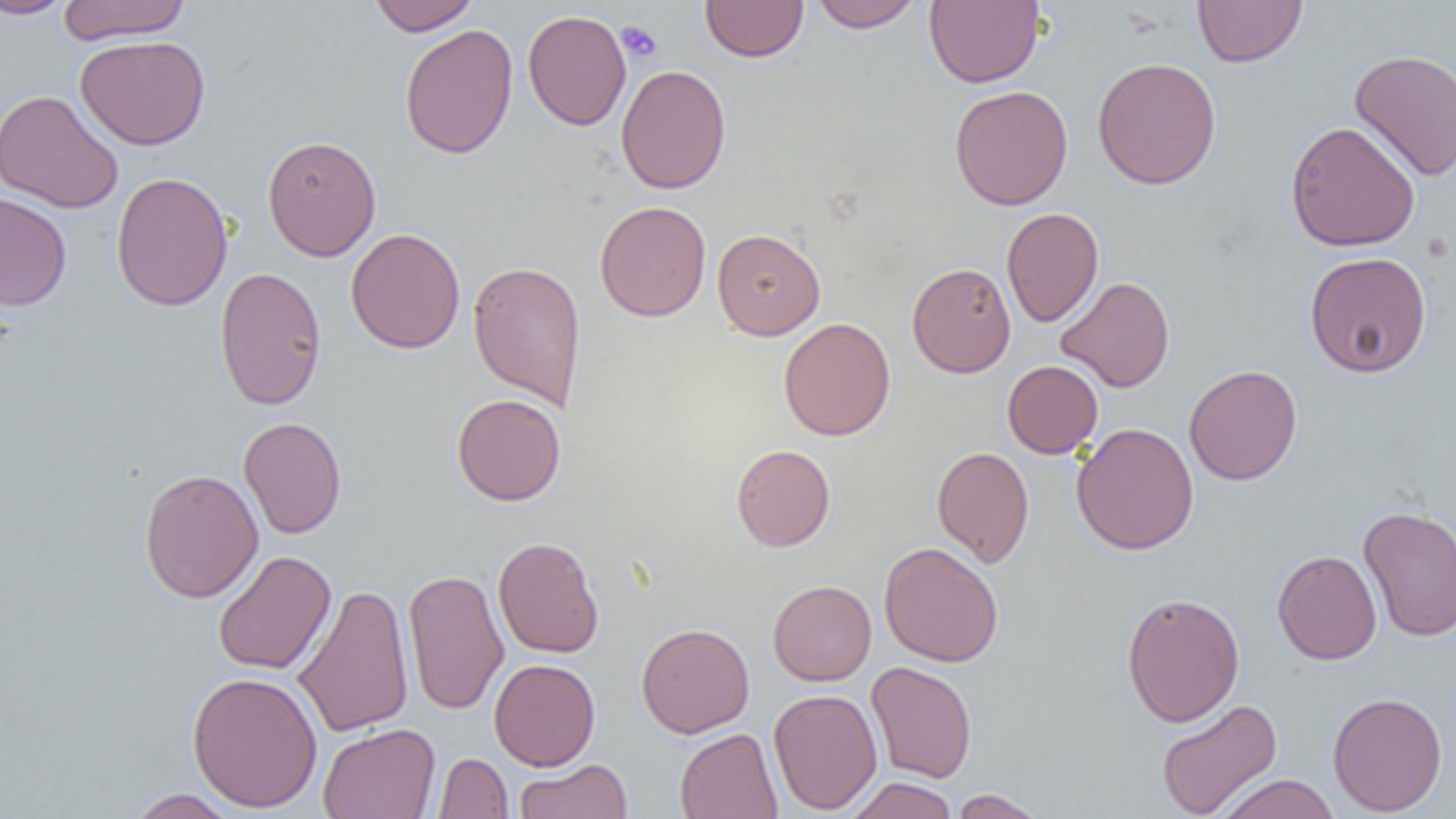

Approximate bounding boxes as [x1, y1, x2, y2] in pixels. Platelet locations: [616, 21, 662, 63]. Uninfected red blood cell locations: [0, 0, 78, 19], [56, 0, 192, 44], [368, 0, 480, 36], [808, 0, 925, 32], [925, 0, 1044, 88], [1193, 0, 1308, 67], [700, 1, 808, 62], [522, 9, 630, 131], [399, 24, 518, 159], [75, 35, 211, 150], [1349, 48, 1456, 182], [1092, 57, 1222, 189], [615, 64, 731, 194], [949, 85, 1073, 210], [0, 90, 124, 213], [1284, 121, 1420, 252], [262, 134, 381, 261], [111, 170, 233, 311], [0, 191, 72, 310], [594, 201, 711, 322], [1002, 208, 1103, 328], [346, 228, 465, 354], [712, 228, 825, 340], [1304, 251, 1432, 378], [467, 259, 587, 410], [907, 262, 1016, 378], [214, 266, 327, 411], [1056, 276, 1175, 393], [778, 317, 895, 441], [1002, 360, 1103, 458], [1184, 365, 1302, 486], [451, 393, 566, 506], [238, 416, 347, 539], [1071, 422, 1199, 555], [731, 444, 835, 552], [932, 445, 1034, 568], [139, 468, 264, 603], [1358, 505, 1456, 642], [493, 536, 604, 658], [878, 541, 1004, 667], [213, 550, 336, 675], [1272, 550, 1382, 665], [403, 568, 509, 716], [767, 580, 877, 686], [293, 582, 414, 738], [1121, 592, 1245, 727], [636, 623, 754, 738], [489, 658, 600, 771], [865, 661, 977, 783], [187, 671, 323, 812], [769, 688, 883, 814], [1328, 691, 1447, 816], [1156, 698, 1283, 818], [317, 723, 440, 819], [675, 728, 782, 818], [433, 752, 513, 818], [514, 758, 633, 818], [1216, 774, 1340, 819], [845, 777, 959, 819], [126, 788, 239, 818], [950, 788, 1048, 818]. Slide-level diagnosis: no evidence of blood parasites. One field of a larger specimen. Thin blood film. Light microscopy. Image is 1456×819 pixels. 1000x magnification.